Outline each blood parasite and name the species.
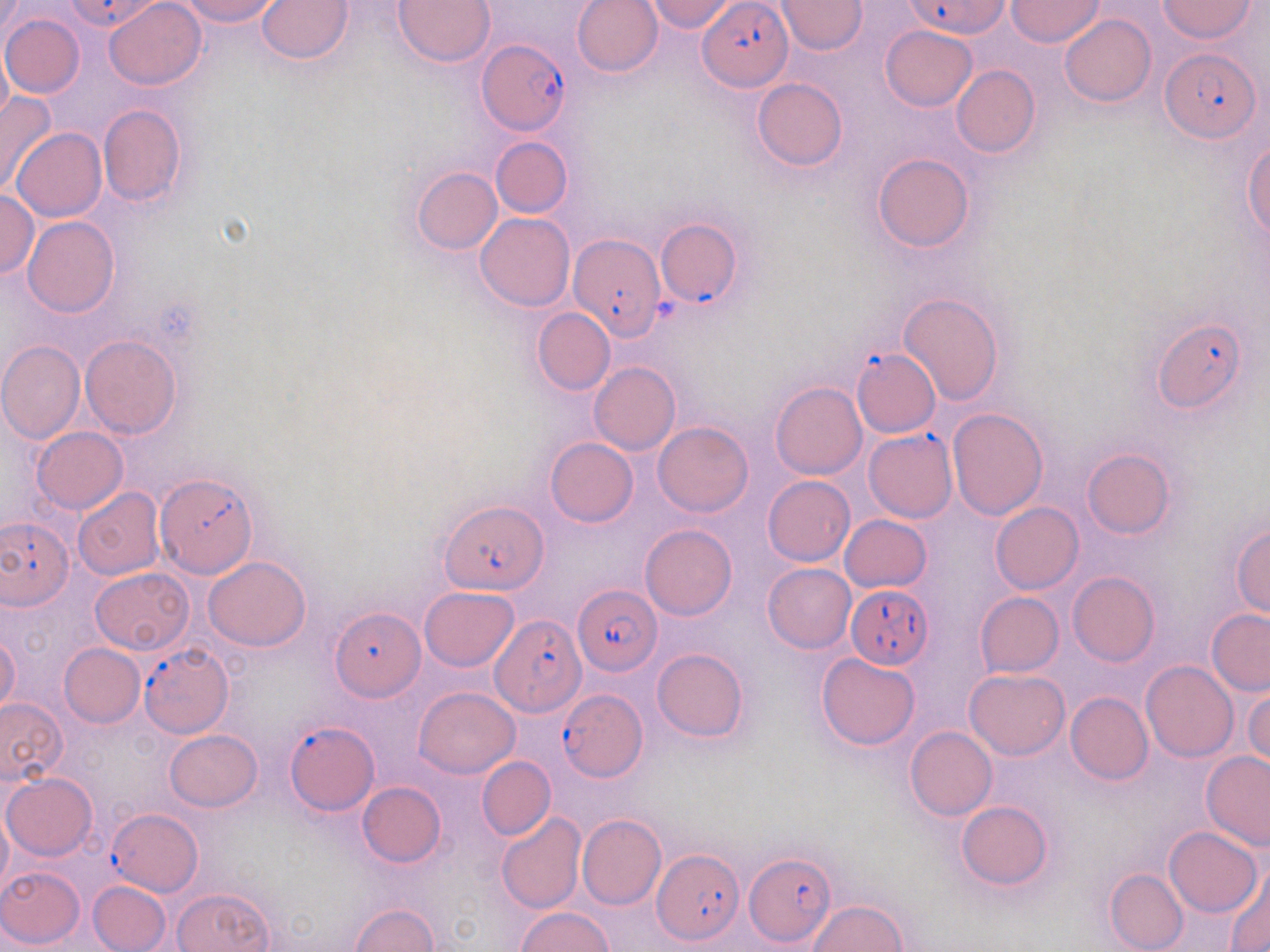
Approximate bounding boxes as (x1, y1, x2, y2) in pixels.
Plasmodium falciparum-infected red blood cells (subset): (64, 0, 165, 33), (904, 0, 1010, 38), (698, 1, 790, 90), (477, 38, 571, 134), (1161, 46, 1260, 144), (655, 218, 742, 308), (570, 233, 665, 340), (1153, 319, 1247, 414), (852, 349, 940, 437), (863, 430, 956, 523), (157, 480, 256, 580), (441, 500, 546, 595), (1, 516, 74, 609), (574, 582, 660, 674), (846, 582, 934, 666), (330, 607, 424, 702), (491, 612, 586, 719), (558, 688, 649, 782), (286, 719, 377, 817), (108, 810, 200, 892), (652, 848, 744, 946), (745, 853, 836, 948).
No Plasmodium ovale, Plasmodium malariae, Plasmodium vivax, Babesia divergens, or Trypanosoma brucei observed.

Uninfected red blood cell locations (subset): (104, 0, 207, 89), (178, 0, 283, 26), (257, 0, 353, 64), (393, 0, 494, 67), (571, 0, 663, 77), (644, 0, 741, 34), (775, 0, 867, 54), (1007, 0, 1103, 47), (1158, 1, 1257, 41), (1, 13, 84, 98), (1059, 13, 1156, 106), (880, 24, 977, 112), (0, 46, 12, 128), (951, 64, 1039, 156), (751, 77, 847, 170), (0, 90, 59, 198), (97, 104, 186, 207), (13, 127, 106, 221), (491, 136, 572, 218), (1244, 141, 1270, 237), (872, 153, 974, 252), (411, 168, 502, 255), (0, 191, 39, 278), (475, 213, 575, 311), (22, 216, 119, 317), (900, 293, 1004, 403), (532, 307, 616, 396), (80, 334, 182, 439), (0, 341, 85, 444), (589, 362, 680, 455), (770, 382, 867, 480), (947, 408, 1047, 520), (653, 422, 752, 517), (31, 427, 128, 514), (544, 437, 638, 527), (1082, 449, 1174, 538), (763, 476, 855, 566), (73, 488, 164, 580), (990, 502, 1084, 594), (838, 515, 932, 593), (641, 524, 737, 621), (1230, 524, 1270, 618), (204, 555, 311, 651), (763, 563, 856, 652), (90, 567, 193, 656), (1068, 572, 1159, 666), (420, 587, 519, 670), (975, 592, 1063, 675), (1206, 609, 1270, 695), (0, 635, 21, 714), (59, 643, 145, 727), (652, 648, 749, 741), (816, 652, 921, 752), (1141, 660, 1238, 763), (965, 669, 1069, 760), (416, 687, 519, 778), (1245, 687, 1270, 768), (1065, 692, 1153, 784), (0, 697, 67, 786), (905, 726, 997, 821), (164, 729, 262, 811), (1200, 750, 1270, 849), (477, 756, 555, 841), (2, 774, 97, 860), (357, 781, 445, 866), (955, 801, 1053, 890), (0, 809, 11, 898), (495, 812, 588, 914), (577, 814, 667, 909), (1164, 826, 1261, 916), (0, 866, 86, 949), (1224, 866, 1270, 951), (1104, 868, 1188, 952), (88, 881, 170, 951), (172, 888, 274, 952), (809, 900, 906, 951), (347, 904, 437, 952), (521, 908, 611, 952). Slide-level diagnosis: Plasmodium falciparum. May-Grünwald-Giemsa stain. 1000x magnification. Image is 1270×952 pixels. Optical microscopy. Single field of view. Thin blood smear.